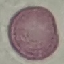
Summary:
  - Result: no malaria parasites detected
  - Capture: smartphone camera at the microscope eyepiece
  - Preparation: thin blood film
  - Image type: cell patch, automatically extracted from a larger field of view and resized to 64 × 64 pixels
  - Stain: Giemsa